State which parasite is depicted.
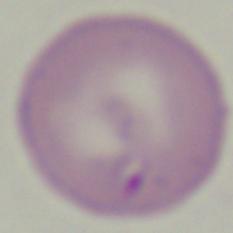
Babesia.

1000x magnification. Micrograph.